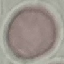
Result: no malaria parasites detected. Cell patch, automatically extracted from a larger field of view and resized to 64 × 64 pixels. Photographed with a smartphone camera at the microscope eyepiece. Thin blood smear. Giemsa-stained preparation.